Identify the parasite.
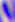
This is Toxoplasma gondii.

Summary:
  - Modality: photomicrograph
  - Magnification: 400x